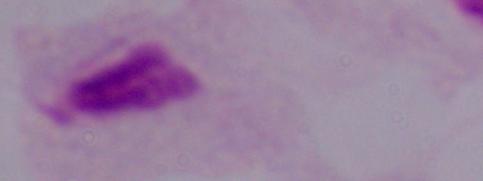 Micrograph. A trichomonad is shown. Captured at 1000x magnification.